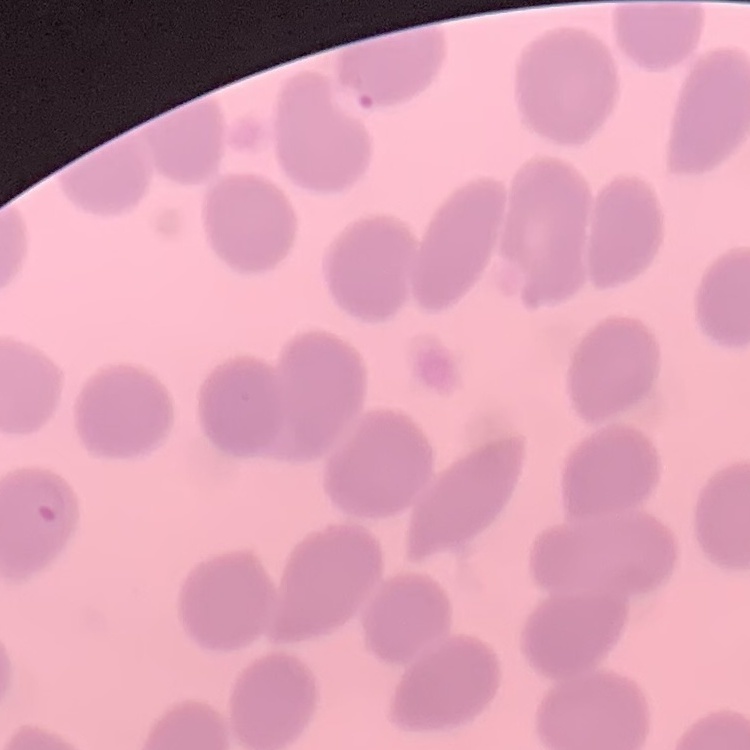
red blood cell morphology = no rouleaux formation
preparation = thin peripheral smear
stain = Field's or Giemsa
image type = square crop of a larger photomicrograph